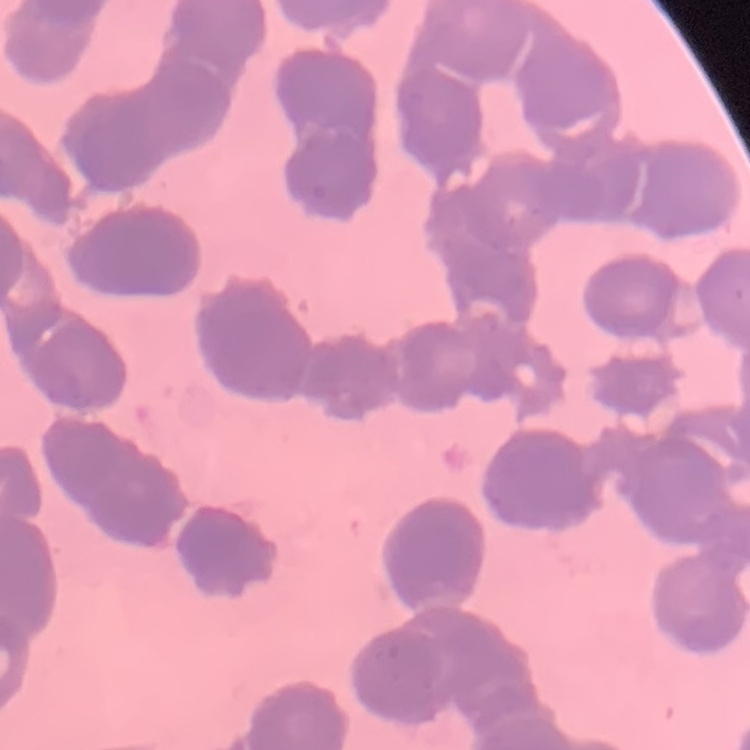
The red blood cells exhibit rouleaux formation. Field's or Giemsa stain. Square crop of a larger photomicrograph. Thin peripheral smear.